Report the malaria status of this cell.
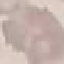
It is uninfected.

Summary:
  - Stain: Giemsa
  - Image type: automatically extracted cell patch, resized to 64 × 64 pixels
  - Capture: smartphone through the microscope eyepiece
  - Preparation: thin blood smear